Give the extent of all Plasmodium falciparum-infected red blood cells.
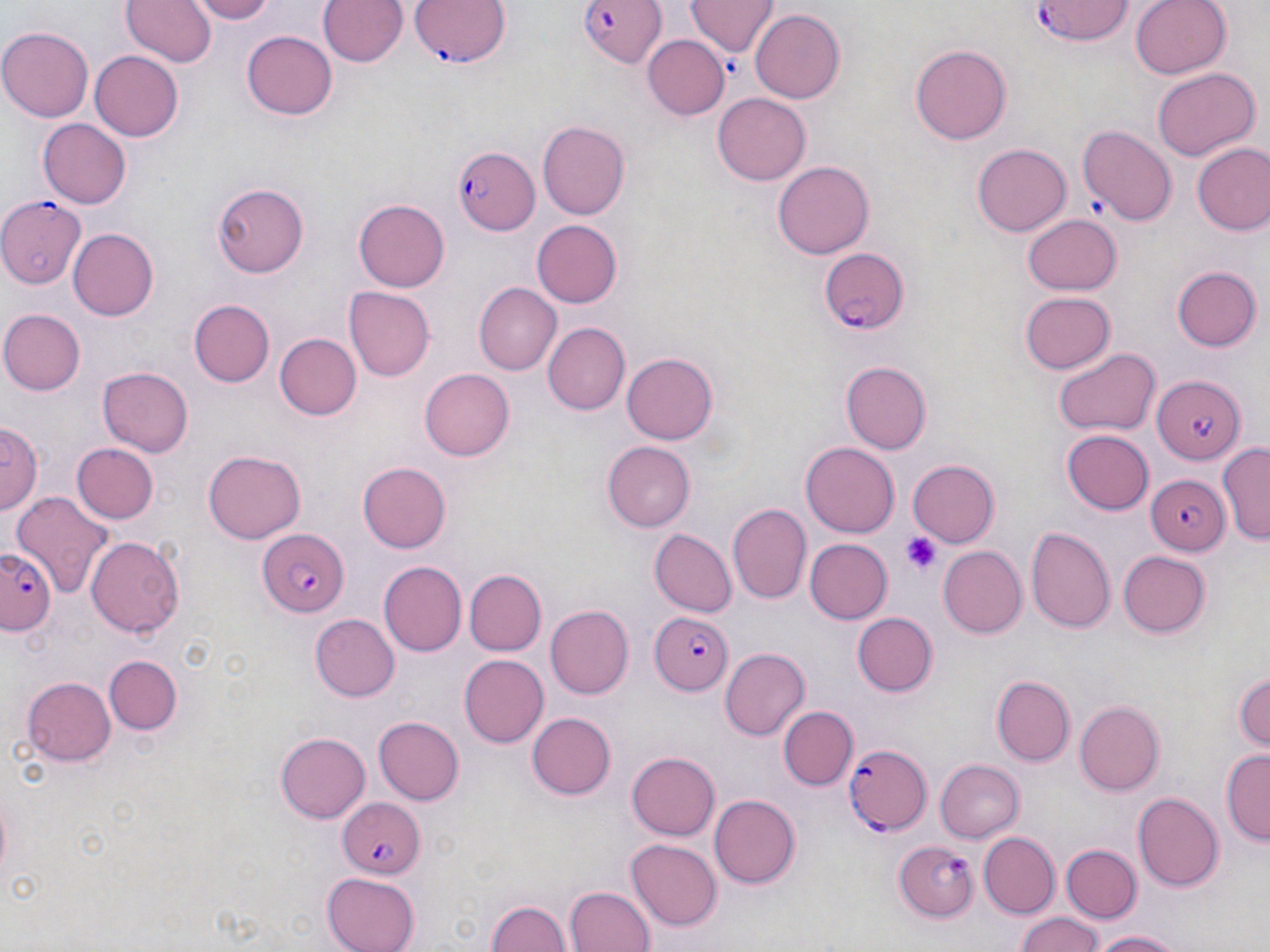

Approximate bounding boxes as (x1,y1)-(x2,y2) corner pairs in pixels.
Plasmodium falciparum-infected red blood cells (subset): (411,0)-(509,69), (1030,1)-(1134,45), (451,147)-(537,233), (0,194)-(84,287), (819,247)-(908,332), (1152,376)-(1244,464), (1146,473)-(1229,553), (258,528)-(349,616), (0,543)-(59,632), (646,609)-(734,694), (845,744)-(931,835), (338,795)-(426,880), (896,839)-(981,921).

slide_level_diagnosis: Plasmodium falciparum
field_of_view: one of a larger specimen
image_size: 1270×952 pixels
preparation: thin blood smear
platelet_locations: 'approximate bounding boxes as (x1,y1)-(x2,y2) corner pairs in pixels: (902,531)-(943,575)'
uninfected_red_blood_cell_locations_subset: 'approximate bounding boxes as (x1,y1)-(x2,y2) corner pairs in pixels: (122,0)-(216,67), (190,0)-(276,24), (319,0)-(408,68), (687,0)-(778,58), (1130,0)-(1232,80), (751,9)-(844,104), (0,25)-(94,122), (242,30)-(337,119), (643,36)-(731,120), (911,45)-(1012,145), (91,51)-(184,141), (1151,68)-(1260,161), (712,93)-(810,185), (39,119)-(132,208), (536,121)-(628,221), (1077,125)-(1177,226), (973,143)-(1071,236), (1191,143)-(1270,236), (772,161)-(874,259), (213,182)-(308,278), (354,200)-(450,290), (1022,213)-(1120,296), (531,219)-(623,309), (69,228)-(158,321), (1171,266)-(1262,352), (472,282)-(561,376), (344,287)-(432,380), (1020,292)-(1115,374), (188,299)-(275,386), (2,310)-(84,395), (543,322)-(629,415), (275,334)-(362,420), (1054,347)-(1160,436), (620,351)-(720,446), (840,360)-(932,454), (98,366)-(195,457), (420,369)-(515,460), (1,422)-(41,517), (1061,430)-(1154,517), (801,439)-(898,535), (603,441)-(694,531), (1216,441)-(1270,545), (73,443)-(159,524), (202,448)-(306,543), (907,459)-(1000,547), (358,460)-(450,550), (12,494)-(116,603), (727,502)-(812,604), (1025,525)-(1117,636), (648,528)-(735,617), (85,531)-(184,636), (803,538)-(892,624), (938,545)-(1026,641), (1118,550)-(1210,638), (378,560)-(467,656), (462,568)-(545,656), (546,606)-(633,697), (853,612)-(937,696), (310,613)-(399,702), (720,648)-(808,740), (105,653)-(182,733), (459,655)-(549,746), (1232,670)-(1270,754), (22,676)-(117,766), (994,676)-(1074,766), (1073,699)-(1164,794), (778,706)-(857,789), (527,713)-(617,800), (374,716)-(463,806), (275,731)-(371,824), (1221,749)-(1269,845), (627,751)-(720,840), (934,759)-(1024,843), (709,791)-(800,886), (1134,791)-(1223,891), (980,831)-(1059,916), (626,839)-(721,931), (1062,843)-(1142,922), (321,872)-(422,952), (565,886)-(654,952), (486,899)-(572,952), (1014,911)-(1105,952), (1088,929)-(1187,952)'
modality: light microscopy
magnification: 1000x
stain: May-Grünwald-Giemsa